Locate every Plasmodium falciparum-infected red blood cell.
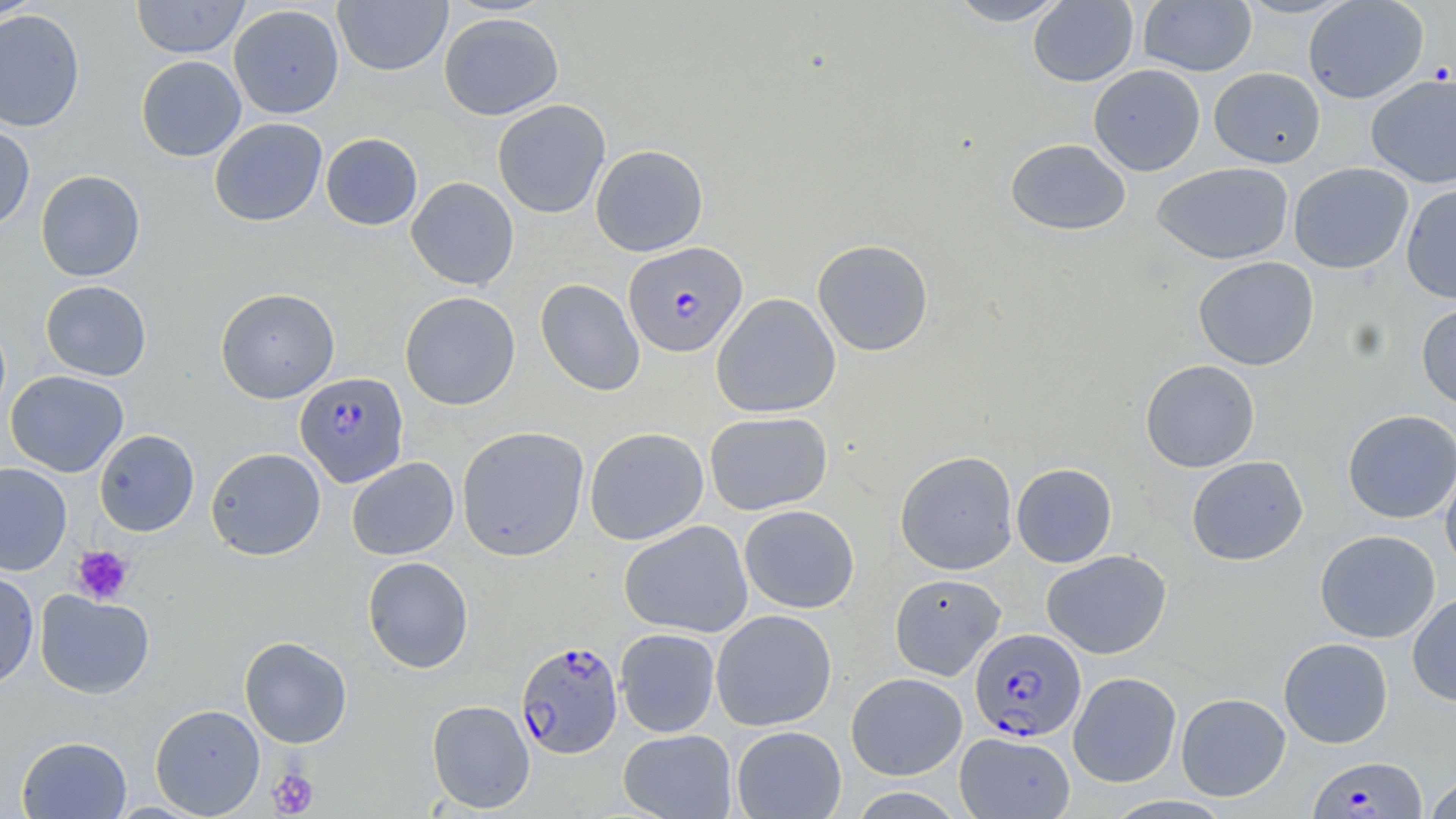
Approximate bounding boxes as named x1/y1/x2/y2 corners in pixels.
Plasmodium falciparum-infected red blood cells: (x1=624, y1=242, x2=747, y2=357), (x1=295, y1=372, x2=409, y2=487), (x1=970, y1=628, x2=1086, y2=742), (x1=515, y1=640, x2=624, y2=758), (x1=1308, y1=756, x2=1428, y2=818).

Summary:
  - Platelet locations: (x1=71, y1=545, x2=135, y2=605), (x1=267, y1=765, x2=320, y2=817)
  - Uninfected red blood cell locations: (x1=131, y1=0, x2=250, y2=58), (x1=943, y1=0, x2=1072, y2=26), (x1=1233, y1=0, x2=1358, y2=19), (x1=1303, y1=0, x2=1429, y2=103), (x1=0, y1=1, x2=47, y2=21), (x1=333, y1=1, x2=452, y2=76), (x1=1028, y1=1, x2=1139, y2=87), (x1=1138, y1=1, x2=1257, y2=76), (x1=228, y1=4, x2=344, y2=119), (x1=0, y1=8, x2=85, y2=133), (x1=439, y1=12, x2=564, y2=121), (x1=136, y1=55, x2=246, y2=161), (x1=1088, y1=64, x2=1205, y2=176), (x1=1209, y1=67, x2=1325, y2=168), (x1=1366, y1=72, x2=1456, y2=188), (x1=492, y1=99, x2=611, y2=218), (x1=209, y1=118, x2=327, y2=226), (x1=0, y1=122, x2=35, y2=231), (x1=321, y1=133, x2=423, y2=230), (x1=1005, y1=138, x2=1131, y2=236), (x1=590, y1=144, x2=708, y2=256), (x1=1151, y1=162, x2=1293, y2=265), (x1=1288, y1=162, x2=1413, y2=274), (x1=35, y1=170, x2=146, y2=281), (x1=406, y1=176, x2=519, y2=290), (x1=1401, y1=185, x2=1456, y2=304), (x1=812, y1=239, x2=934, y2=356), (x1=1193, y1=257, x2=1319, y2=371), (x1=535, y1=279, x2=645, y2=396), (x1=40, y1=280, x2=152, y2=381), (x1=215, y1=287, x2=340, y2=403), (x1=399, y1=291, x2=521, y2=410), (x1=712, y1=293, x2=841, y2=418), (x1=1416, y1=300, x2=1456, y2=410), (x1=1140, y1=359, x2=1260, y2=473), (x1=5, y1=370, x2=129, y2=477), (x1=1342, y1=409, x2=1456, y2=524), (x1=704, y1=411, x2=833, y2=515), (x1=720, y1=413, x2=846, y2=612), (x1=456, y1=426, x2=589, y2=561), (x1=584, y1=427, x2=709, y2=545), (x1=94, y1=429, x2=200, y2=536), (x1=205, y1=447, x2=326, y2=560), (x1=894, y1=450, x2=1018, y2=575), (x1=1186, y1=455, x2=1309, y2=566), (x1=346, y1=456, x2=459, y2=560), (x1=1440, y1=456, x2=1456, y2=575), (x1=0, y1=462, x2=72, y2=576), (x1=1011, y1=462, x2=1117, y2=567), (x1=739, y1=505, x2=860, y2=614), (x1=619, y1=520, x2=754, y2=638), (x1=1315, y1=529, x2=1440, y2=643), (x1=1041, y1=549, x2=1172, y2=659), (x1=362, y1=556, x2=474, y2=673), (x1=0, y1=571, x2=39, y2=690), (x1=888, y1=573, x2=1006, y2=680), (x1=35, y1=590, x2=154, y2=698), (x1=1407, y1=592, x2=1456, y2=706), (x1=711, y1=609, x2=837, y2=731), (x1=614, y1=628, x2=721, y2=737), (x1=239, y1=636, x2=352, y2=748), (x1=1278, y1=637, x2=1393, y2=748), (x1=1068, y1=671, x2=1181, y2=788), (x1=846, y1=672, x2=967, y2=780), (x1=1176, y1=692, x2=1291, y2=801), (x1=426, y1=700, x2=535, y2=813), (x1=150, y1=704, x2=265, y2=817), (x1=731, y1=725, x2=846, y2=818), (x1=618, y1=729, x2=737, y2=818), (x1=954, y1=731, x2=1075, y2=819), (x1=17, y1=735, x2=132, y2=818), (x1=1423, y1=773, x2=1456, y2=818)
  - Slide-level diagnosis: Plasmodium falciparum
  - Magnification: 1000x
  - Field of view: one of a larger specimen
  - Image size: 1456×819 pixels
  - Preparation: thin blood smear
  - Modality: light microscopy
  - Stain: May-Grünwald-Giemsa